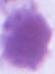

identification = erythrocyte
modality = photomicrograph
magnification = 1000x